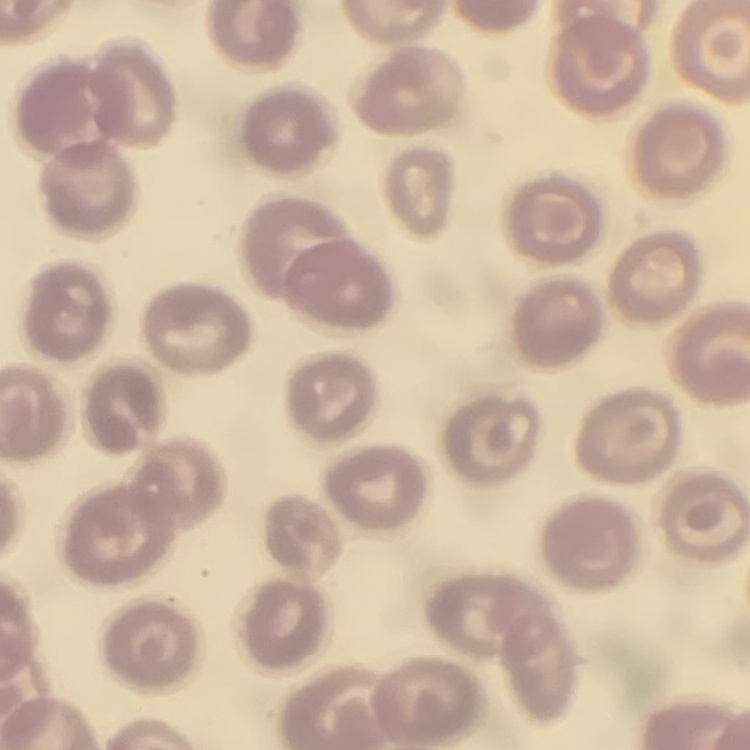

erythrocyte_morphology: no rouleaux formation
stain: Field's or Giemsa
preparation: thin blood film
image_type: square crop of a larger photomicrograph